Describe the morphology of the erythrocytes.
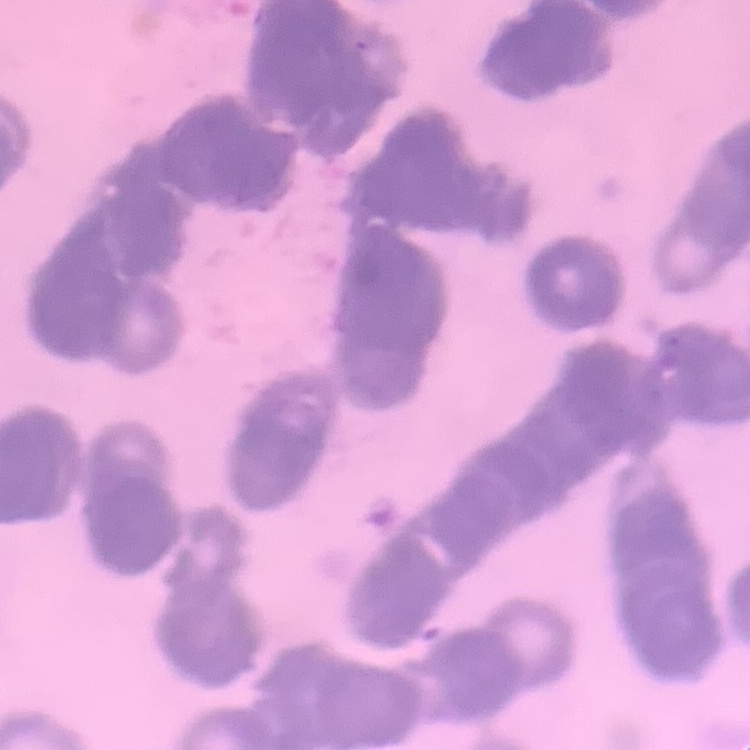

Rouleaux formation.

stain = Field's or Giemsa
image type = one tile cut from a larger photomicrograph
preparation = thin blood film